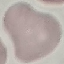
Summary:
  - Malaria status: uninfected
  - Capture: smartphone camera at the microscope eyepiece
  - Stain: Giemsa
  - Preparation: thin smear
  - Image type: automatically extracted cell patch, resized to 64 × 64 pixels